Assess the morphology of the red blood cells.
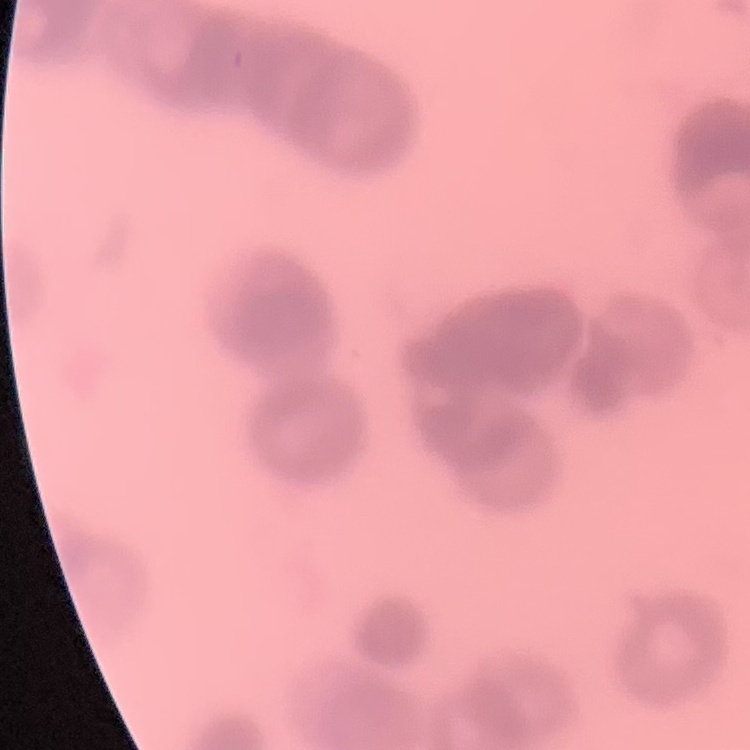
They show rouleaux formation.

Square crop of a larger photomicrograph. Field's or Giemsa stain. Thin blood film.